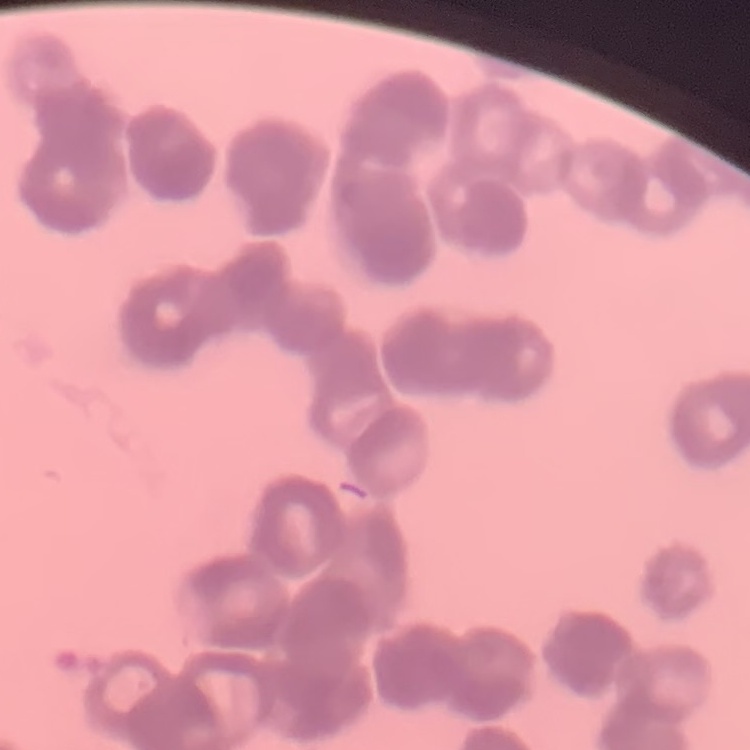

Summary:
  - Erythrocyte morphology: rouleaux formation
  - Stain: Field's or Giemsa
  - Preparation: thin peripheral smear
  - Image type: square crop of a larger photomicrograph